State which parasite is depicted.
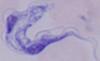
A trypanosome.

magnification = 1000x
modality = photomicrograph